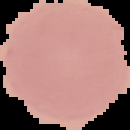
Summary:
  - Image type: segmented cell region on a black background
  - Preparation: thin blood film
  - Malaria status: uninfected
  - Image size: 130×130 pixels